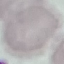

Summary:
  - Result: no malaria parasites detected
  - Image type: automatically extracted cell patch, resized to 64 × 64 pixels
  - Preparation: thin blood film
  - Capture: smartphone camera at the microscope eyepiece
  - Stain: Giemsa